Evaluate for Plasmodium parasites.
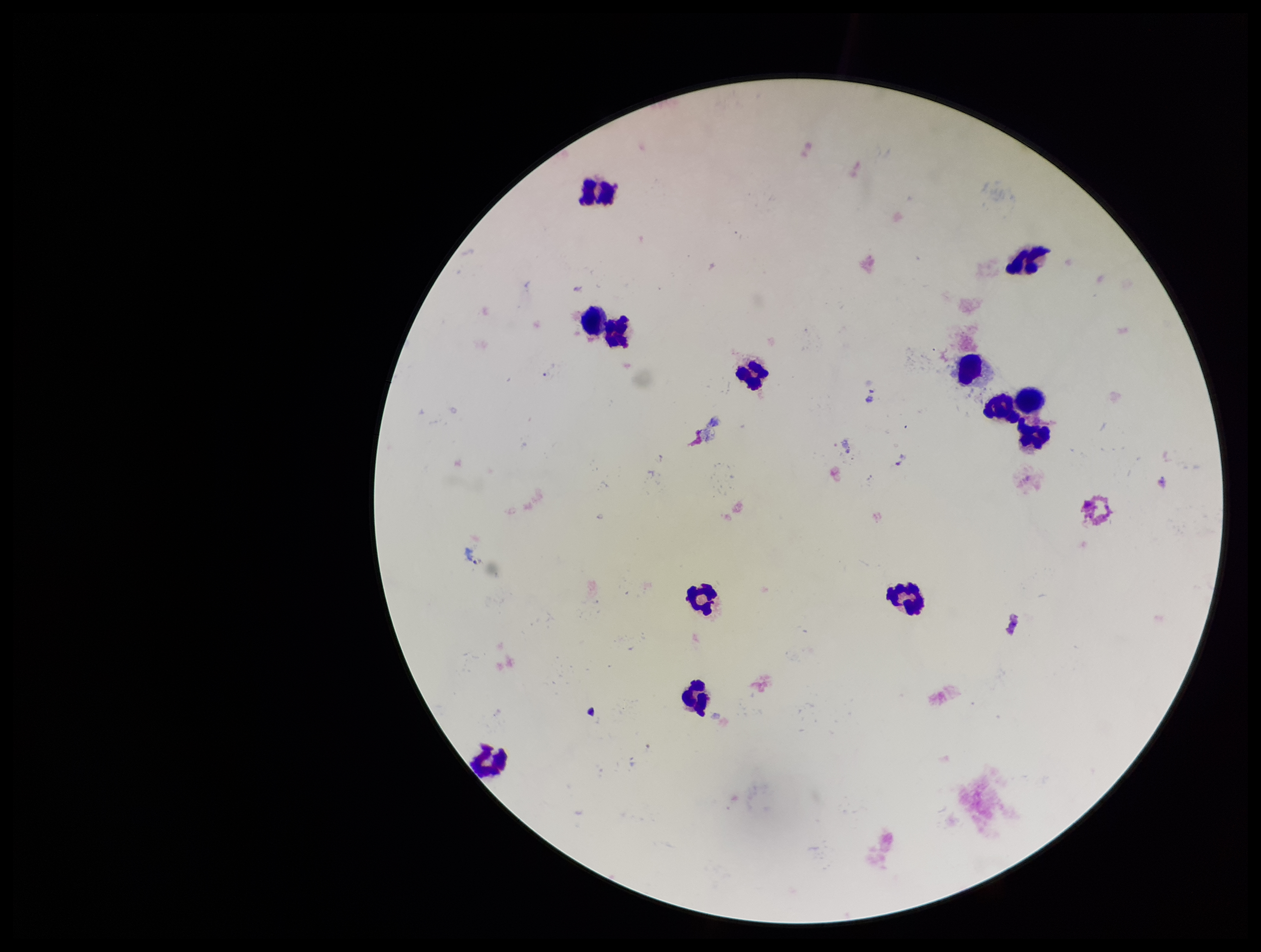

None seen.

Leukocyte count: 13. Giemsa stain. Preparation: thick blood smear. Image is 1261×952 pixels. One field from this slide. Smartphone photograph taken through the eyepiece of a microscope. Parasite count: 0. Patient malaria status: negative.